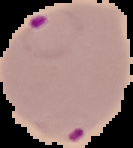

Summary:
  - Result: Plasmodium parasites identified
  - Preparation: thin blood film
  - Image type: segmented cell region on a black background
  - Image size: 133×148 pixels